Locate every uninfected red blood cell.
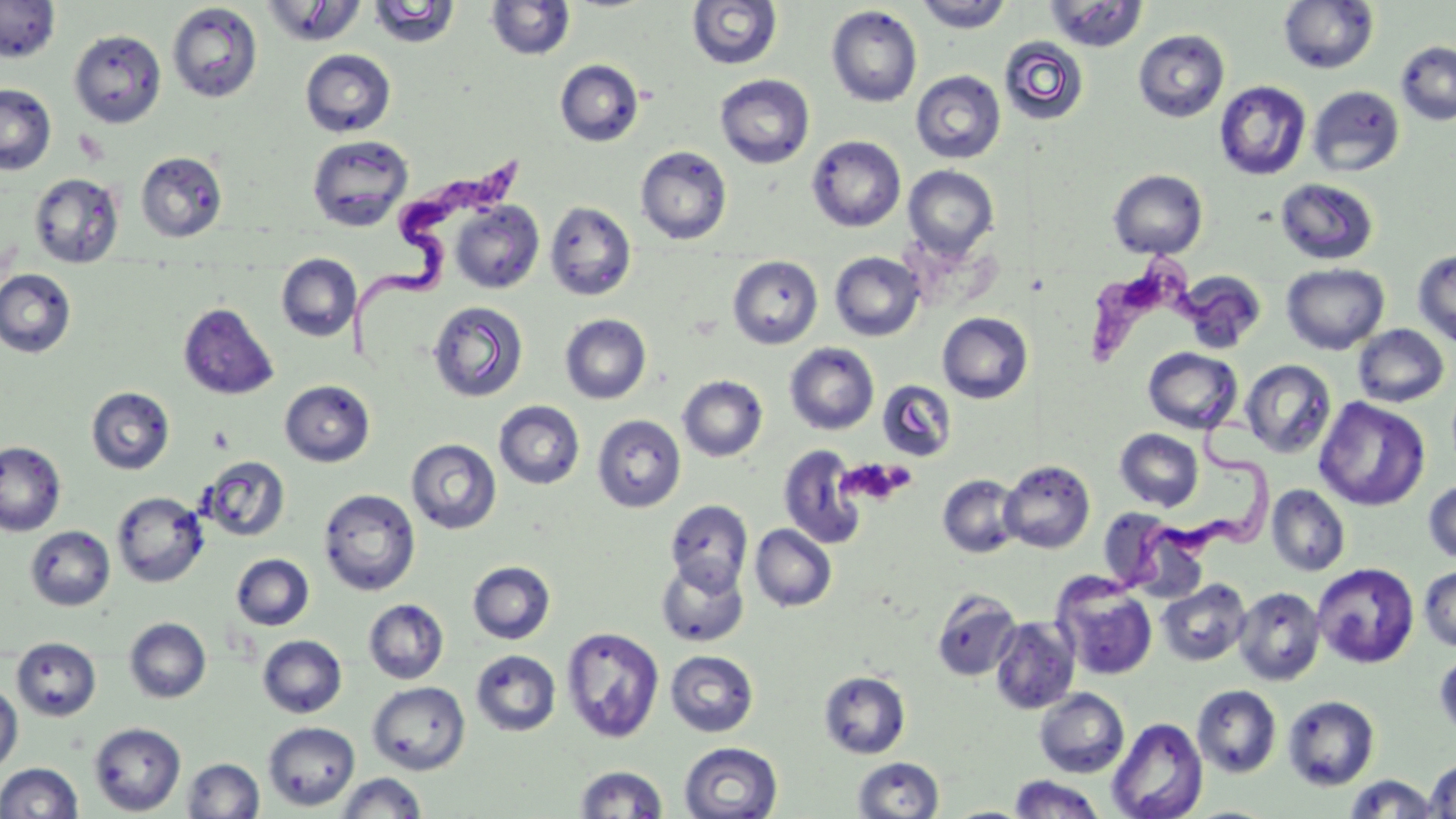

Approximate bounding boxes as (x1, y1, x2, y2) in pixels.
Uninfected red blood cells: (0, 0, 61, 62), (915, 0, 1014, 33), (260, 1, 368, 47), (486, 1, 577, 61), (686, 1, 782, 70), (1045, 1, 1149, 52), (1278, 1, 1380, 74), (367, 2, 460, 48), (166, 3, 263, 103), (826, 5, 922, 108), (69, 29, 167, 128), (1133, 29, 1230, 123), (999, 36, 1090, 126), (1396, 40, 1456, 126), (300, 49, 396, 138), (554, 59, 644, 147), (910, 70, 1006, 164), (715, 74, 815, 169), (1214, 81, 1311, 181), (0, 83, 57, 175), (1307, 85, 1405, 177), (307, 135, 414, 232), (807, 135, 906, 232), (635, 146, 732, 244), (136, 151, 227, 242), (903, 165, 999, 259), (1108, 169, 1208, 259), (29, 173, 124, 268), (1275, 177, 1379, 265), (450, 201, 544, 293), (545, 201, 637, 301), (1413, 248, 1456, 347), (830, 252, 925, 341), (276, 253, 361, 342), (727, 255, 823, 349), (1281, 263, 1389, 354), (0, 269, 76, 358), (1178, 271, 1266, 353), (427, 301, 528, 403), (178, 303, 279, 401), (938, 312, 1033, 403), (560, 314, 652, 404), (1352, 324, 1450, 407), (784, 342, 879, 435), (1143, 347, 1242, 433), (1241, 360, 1336, 458), (677, 375, 768, 462), (280, 380, 375, 467), (877, 380, 956, 462), (86, 387, 175, 475), (1314, 397, 1430, 511), (494, 401, 585, 489), (592, 415, 686, 512), (1115, 428, 1203, 511), (406, 439, 501, 534), (0, 441, 66, 536), (778, 445, 867, 550), (199, 456, 290, 542), (1000, 459, 1095, 553), (937, 474, 1024, 558), (1423, 479, 1456, 564), (1267, 484, 1350, 576), (318, 488, 421, 596), (112, 491, 208, 587), (664, 499, 753, 593), (1101, 514, 1207, 600), (750, 524, 837, 612), (25, 526, 115, 611), (231, 554, 314, 630), (656, 558, 749, 647), (468, 561, 555, 644), (1312, 562, 1419, 668), (1419, 565, 1456, 653), (1053, 576, 1158, 682), (1158, 579, 1251, 666), (1233, 586, 1326, 686), (932, 590, 1021, 681), (363, 599, 449, 684), (124, 617, 211, 703), (990, 617, 1081, 714), (561, 626, 665, 744), (258, 635, 347, 718), (12, 637, 102, 721), (471, 649, 561, 736), (666, 650, 758, 737), (1434, 650, 1456, 739), (819, 671, 910, 759), (367, 681, 471, 775), (0, 682, 23, 773), (1192, 685, 1281, 778), (1034, 688, 1129, 778), (1283, 695, 1380, 791), (1107, 717, 1208, 819), (263, 721, 360, 811), (88, 723, 186, 815), (679, 741, 782, 819), (852, 757, 945, 818), (182, 758, 265, 818), (1425, 760, 1456, 818), (1, 762, 83, 819), (574, 765, 668, 818), (335, 772, 427, 818), (1344, 774, 1440, 818), (1008, 775, 1106, 818), (944, 805, 1029, 818).

Summary:
  - Platelet locations: (209, 426, 235, 452), (838, 459, 913, 507)
  - Trypanosoma brucei locations: (351, 144, 532, 355), (1085, 249, 1267, 368), (1110, 412, 1282, 597)
  - Slide-level diagnosis: Trypanosoma brucei
  - Stain: May-Grünwald-Giemsa
  - Field of view: single
  - Image size: 1456×819 pixels
  - Magnification: 1000x
  - Preparation: thin blood film
  - Modality: optical microscopy